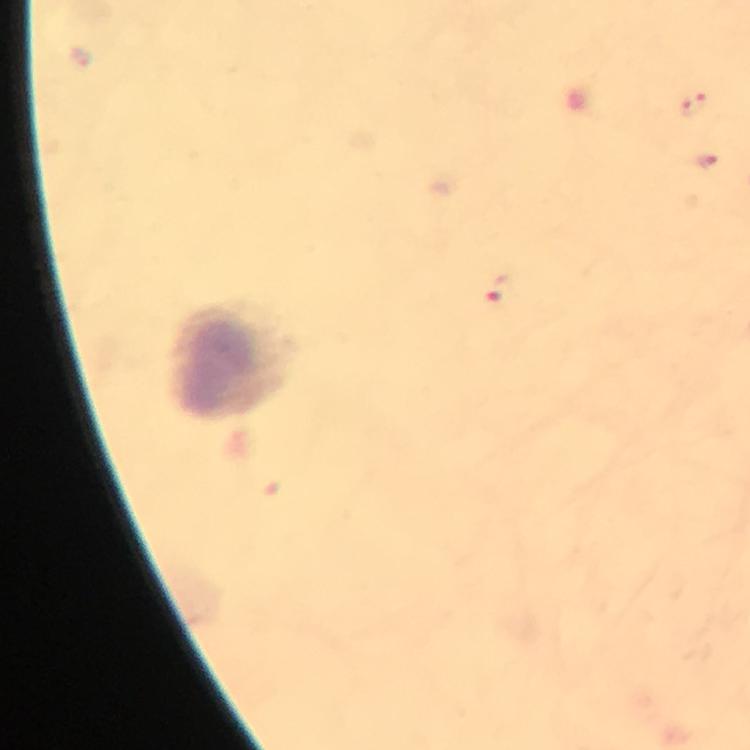
leukocyte_locations: 'approximate centers as [x, y] in pixels: [229, 361]'
immersion_oil: used
capture: smartphone camera through the microscope
cropped_from: one field of view
stain: Giemsa
magnification: 100x
context: from a diagnostic examination for malaria
preparation: thick smear
image_size: 750×750 pixels
plasmodium_parasite_locations: 'approximate centers as [x, y] in pixels: [693, 104], [704, 160], [498, 287]'